Locate every malaria parasite and every leukocyte.
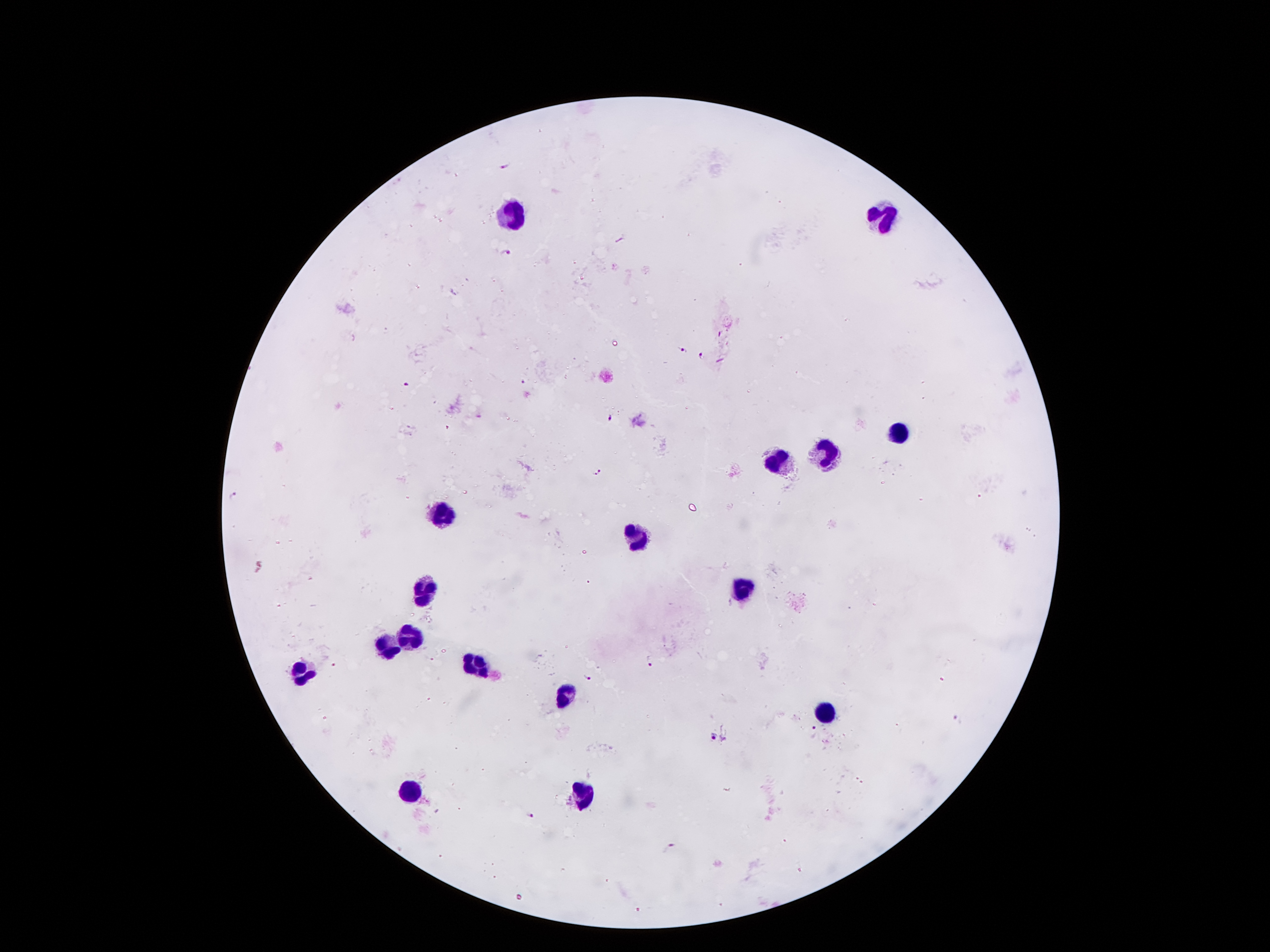
Approximate centers as {x, y} in pixels.
Malaria parasites: {504, 166}, {509, 251}, {684, 351}, {702, 354}, {524, 382}, {407, 385}, {478, 415}, {612, 419}, {598, 472}, {234, 497}, {651, 662}, {335, 665}, {590, 677}, {957, 719}, {814, 731}, {714, 737}, {723, 739}, {533, 816}, {669, 846}.
Leukocytes: {508, 211}, {883, 214}, {895, 432}, {828, 451}, {776, 458}, {441, 514}, {639, 536}, {421, 588}, {742, 592}, {409, 636}, {385, 647}, {473, 664}, {301, 672}, {565, 698}, {827, 712}, {412, 790}, {583, 794}.

Summary:
  - Capture: smartphone through the microscope eyepiece
  - Image size: 1270×952 pixels
  - Patient malaria status: infected with Plasmodium falciparum
  - Stain: Giemsa
  - Preparation: thick blood smear
  - Magnification: 100x
  - Field of view: one from this slide